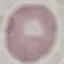

malaria_status: uninfected
stain: Giemsa
image_type: cell patch, automatically extracted from a larger field of view and resized to 64 × 64 pixels
capture: smartphone through the microscope eyepiece
preparation: thin smear